Assess this cell for malaria.
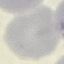
Uninfected.

Summary:
  - Preparation: thin smear
  - Stain: Giemsa
  - Image type: automatically extracted cell patch, resized to 64 × 64 pixels
  - Capture: smartphone through the microscope eyepiece